Comment on the morphology of the red blood cells.
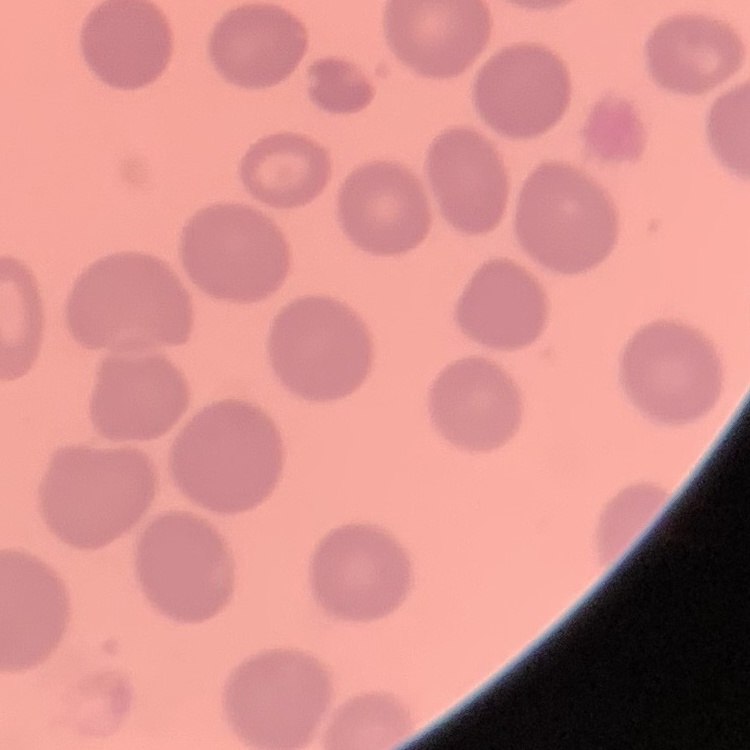

No rouleaux formation.

Field's or Giemsa stain. Thin blood smear. Square crop of a larger photomicrograph.